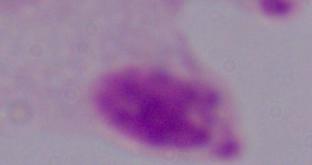

Summary:
  - Identification: trichomonad
  - Magnification: 1000x
  - Modality: photomicrograph